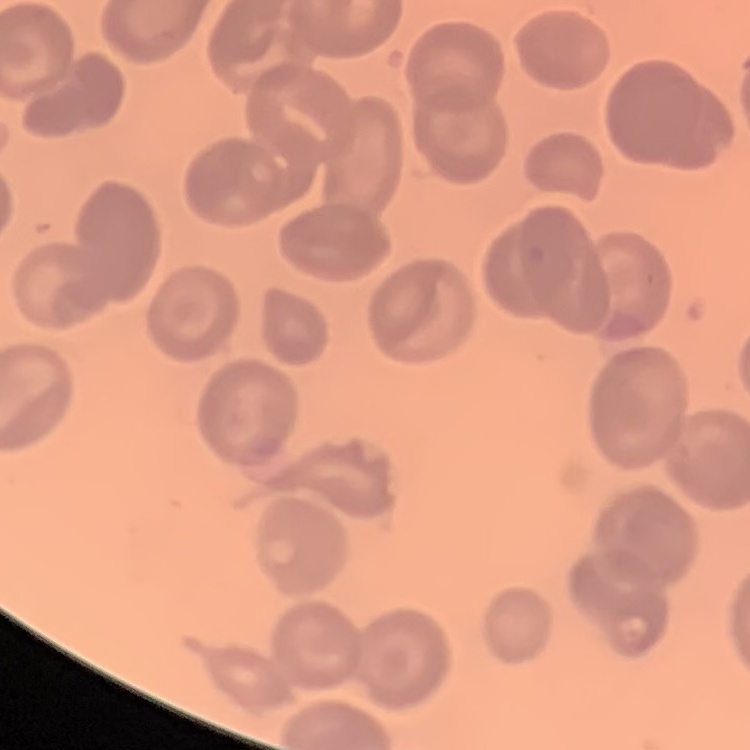 The red blood cells show no rouleaux formation. One tile cut from a larger photomicrograph. Stained with either Field's or Giemsa. Thin blood film.